Name the blood parasite species.
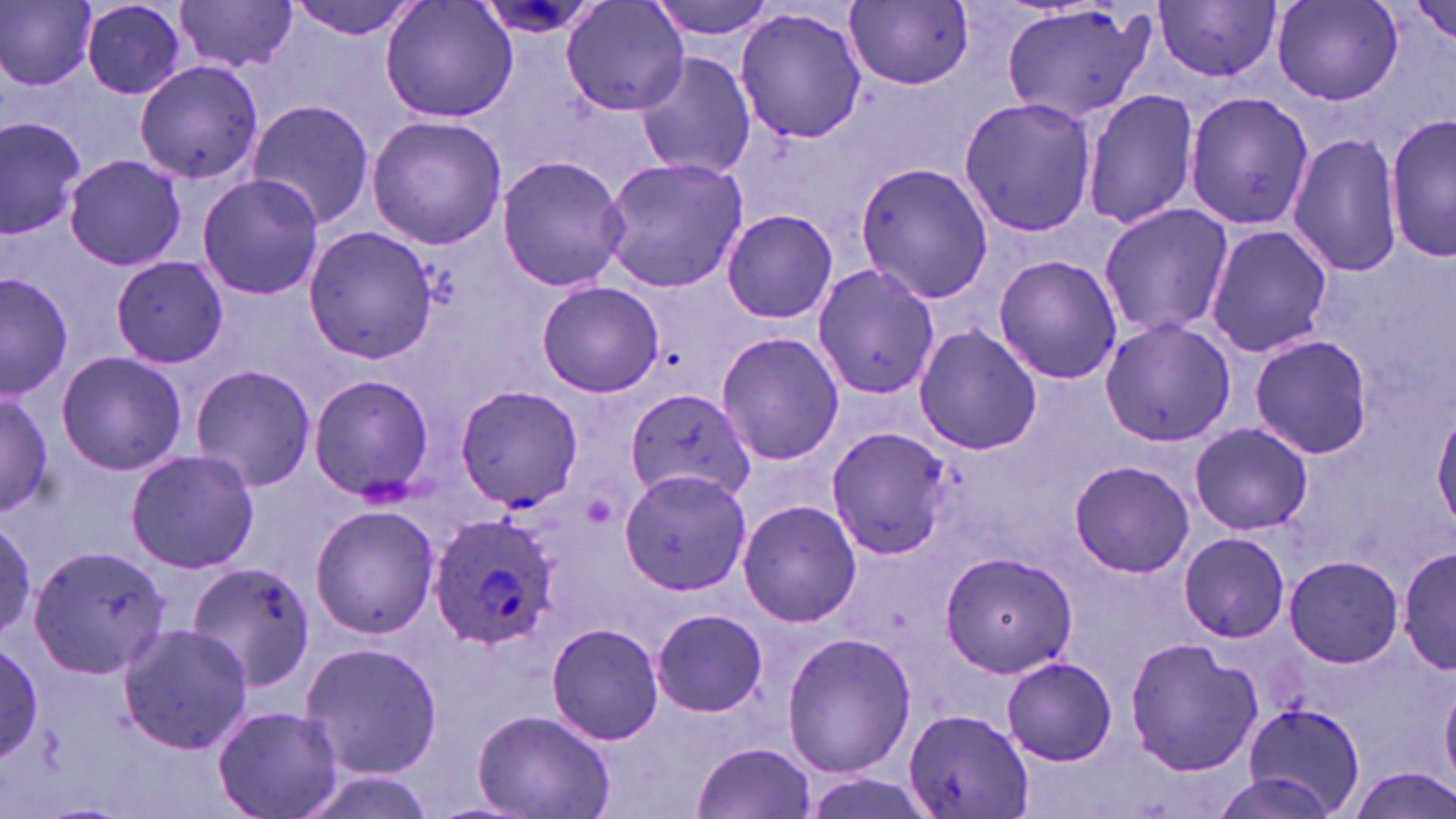
Plasmodium ovale.

Summary:
  - Coordinate format: approximate bounding boxes as (x1,y1)-(x2,y2) corner pairs in pixels
  - Plasmodium ovale-infected red blood cell locations: (427,513)-(560,652)
  - Uninfected red blood cell locations: (1,0)-(99,90), (175,0)-(299,74), (285,0)-(425,41), (380,0)-(517,123), (560,0)-(690,117), (645,0)-(780,40), (1157,1)-(1282,82), (1272,1)-(1403,107), (79,2)-(187,101), (1408,2)-(1453,48), (840,3)-(973,92), (1002,3)-(1155,126), (735,5)-(867,143), (634,52)-(759,181), (135,62)-(264,185), (1083,91)-(1199,231), (1182,91)-(1315,231), (958,96)-(1099,236), (245,98)-(374,230), (1387,113)-(1455,262), (0,114)-(89,241), (367,115)-(508,249), (1287,129)-(1405,278), (64,154)-(187,272), (495,155)-(630,292), (596,156)-(751,292), (853,161)-(992,305), (196,173)-(327,301), (1098,202)-(1235,340), (720,208)-(839,325), (1206,224)-(1332,356), (304,226)-(440,363), (110,254)-(228,369), (994,256)-(1123,385), (811,262)-(942,400), (0,270)-(73,403), (537,281)-(663,398), (1100,318)-(1237,448), (914,323)-(1041,456), (716,332)-(845,467), (1248,336)-(1374,459), (54,350)-(188,476), (189,363)-(318,494), (308,375)-(435,502), (454,384)-(583,510), (626,387)-(757,503), (0,389)-(55,517), (1433,406)-(1456,534), (1189,422)-(1313,534), (826,425)-(951,559), (124,449)-(260,573), (1067,460)-(1198,578), (620,468)-(752,592), (736,498)-(862,628), (309,502)-(442,639), (0,513)-(38,645), (1177,531)-(1290,642), (1399,541)-(1453,678), (27,543)-(173,679), (938,552)-(1080,678), (1285,554)-(1402,670), (182,561)-(316,693), (651,609)-(768,717), (546,622)-(664,746), (118,624)-(256,755), (781,632)-(916,777), (1124,636)-(1261,777), (299,641)-(444,778), (0,643)-(47,762), (1001,656)-(1118,767), (228,668)-(424,808), (1441,672)-(1456,786), (1244,704)-(1366,819), (210,707)-(344,819), (903,708)-(1032,819), (473,710)-(615,819), (692,740)-(817,819), (290,765)-(448,819), (1344,765)-(1456,819)
  - Magnification: 1000x
  - Modality: light microscopy
  - Preparation: thin blood smear
  - Image size: 1456×819 pixels
  - Field of view: single
  - Stain: May-Grünwald-Giemsa